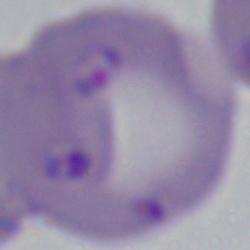
Summary:
  - Magnification: 1000x
  - Identification: Babesia
  - Modality: photomicrograph